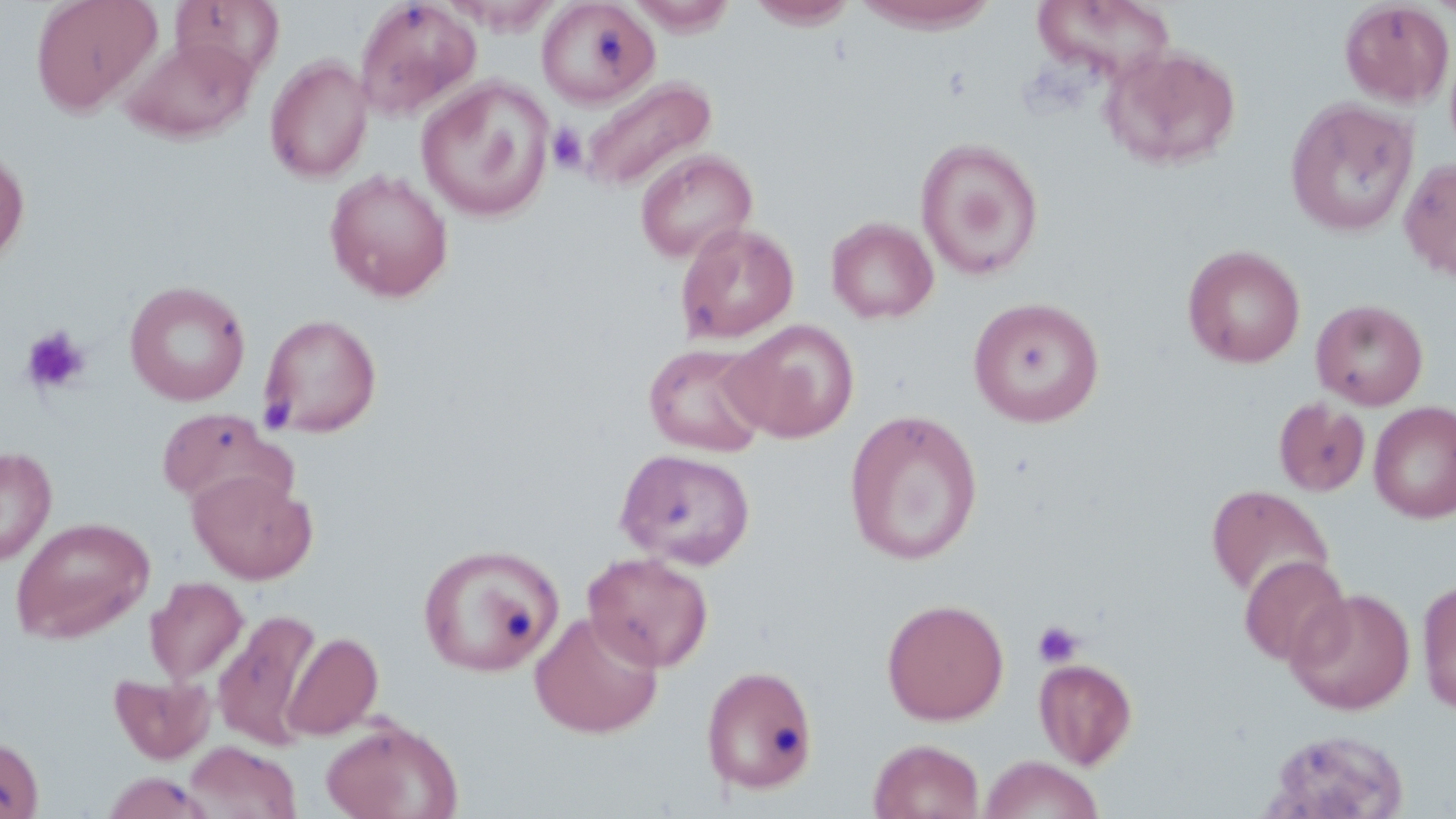

Summary:
  - Coordinate format: approximate bounding boxes as [x1, y1, x2, y2] in pixels
  - Uninfected red blood cell locations: [31, 0, 162, 117], [171, 0, 284, 81], [536, 0, 660, 110], [747, 0, 859, 29], [852, 0, 1003, 33], [354, 1, 482, 121], [628, 1, 740, 37], [1030, 1, 1179, 84], [1339, 1, 1454, 108], [1430, 1, 1456, 22], [122, 37, 258, 144], [1101, 45, 1242, 171], [264, 56, 373, 183], [416, 76, 554, 223], [579, 76, 717, 194], [1285, 98, 1419, 237], [916, 137, 1044, 281], [0, 143, 30, 269], [634, 149, 758, 264], [1399, 157, 1456, 282], [325, 169, 454, 302], [826, 217, 939, 324], [675, 221, 799, 345], [1182, 245, 1306, 369], [124, 280, 251, 406], [968, 296, 1105, 428], [1311, 298, 1428, 410], [259, 313, 382, 438], [724, 318, 859, 443], [643, 342, 771, 457], [1273, 398, 1370, 497], [1369, 401, 1455, 523], [156, 407, 292, 509], [843, 409, 983, 566], [0, 446, 57, 567], [616, 448, 756, 569], [188, 470, 318, 585], [1206, 484, 1334, 601], [11, 516, 155, 643], [418, 543, 564, 677], [582, 552, 714, 672], [1239, 555, 1351, 667], [145, 577, 248, 685], [1417, 579, 1456, 715], [1286, 587, 1416, 714], [881, 597, 1010, 726], [213, 610, 322, 751], [530, 610, 664, 738], [283, 632, 383, 740], [1033, 657, 1137, 769], [701, 664, 819, 796], [109, 672, 216, 764], [321, 718, 463, 819], [1265, 729, 1408, 818], [0, 736, 44, 819], [868, 738, 985, 819], [185, 741, 301, 819], [980, 754, 1103, 819], [101, 772, 216, 819]
  - Platelet locations: [547, 124, 587, 173], [21, 325, 91, 396], [1032, 620, 1084, 669]
  - Slide-level diagnosis: negative for blood parasites
  - Image size: 1456×819 pixels
  - Field of view: one of a larger specimen
  - Magnification: 1000x
  - Stain: May-Grünwald-Giemsa
  - Preparation: thin blood film
  - Modality: optical microscopy